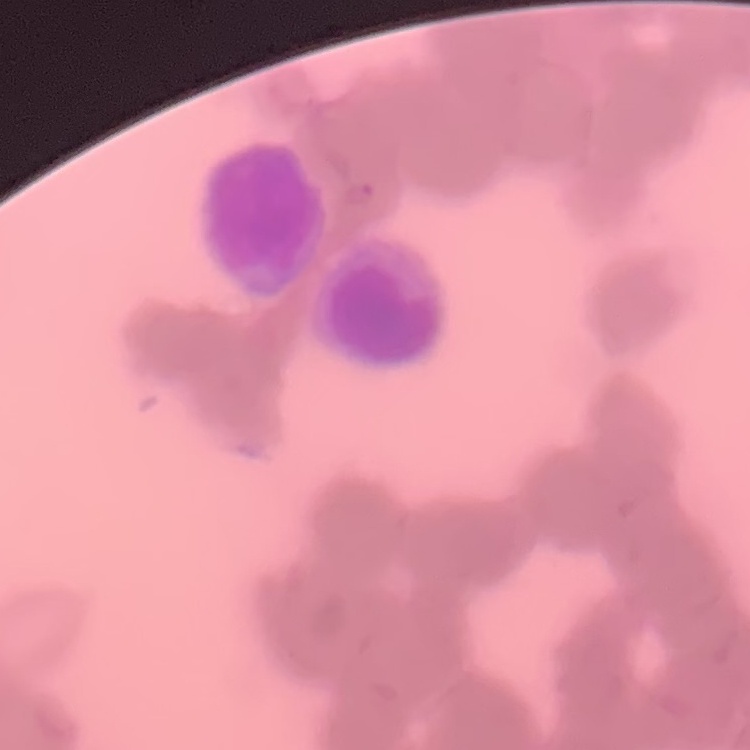

The erythrocytes exhibit rouleaux formation. Stained with either Field's or Giemsa. Square crop of a larger photomicrograph. Thin blood film.